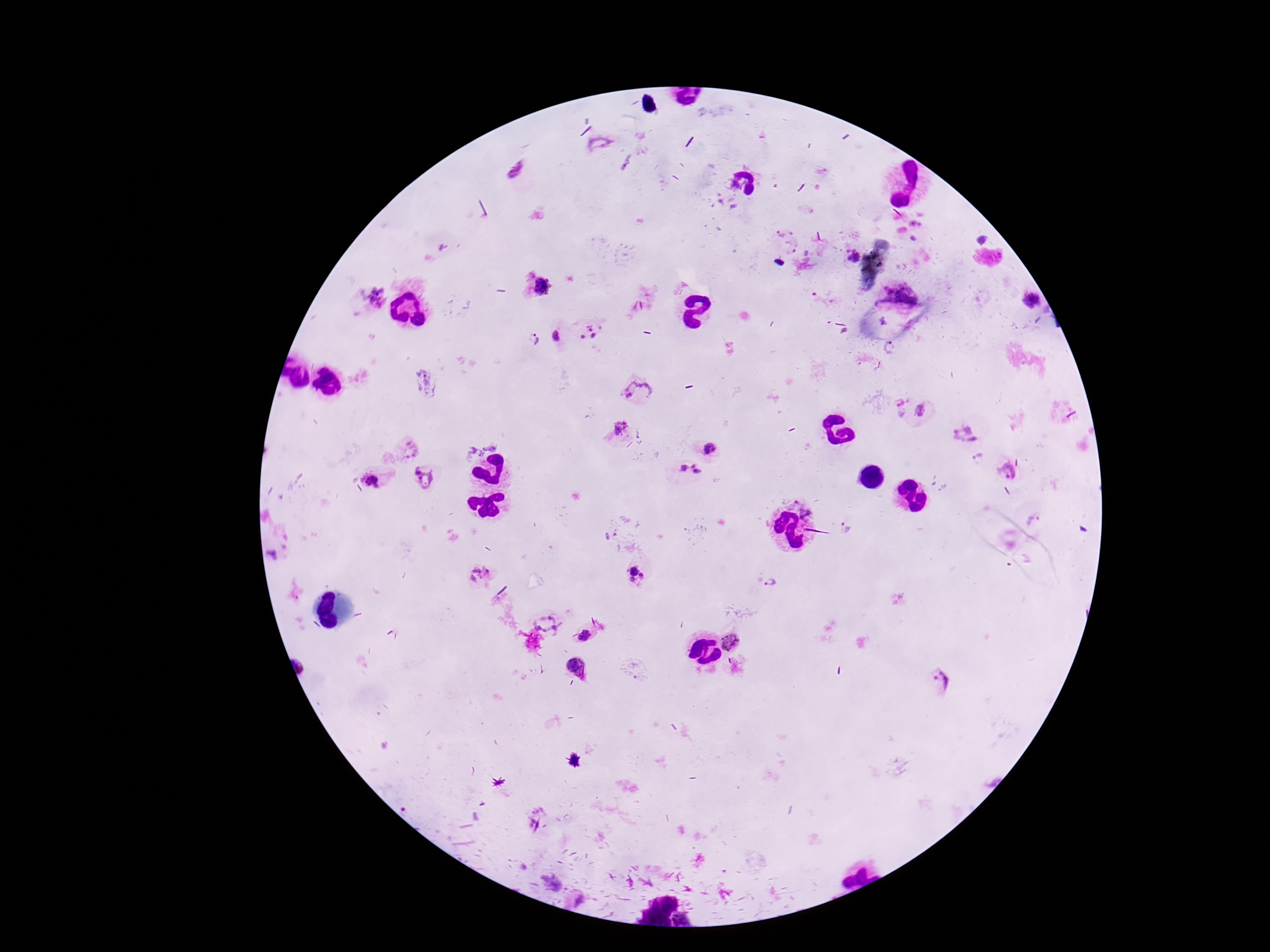
Approximate centers as {x, y} in pixels.
Summary:
  - Plasmodium parasite locations: {518, 171}, {984, 237}, {787, 243}, {851, 257}, {540, 287}, {375, 297}, {1031, 300}, {590, 331}, {557, 336}, {536, 339}, {889, 348}, {637, 390}, {901, 406}, {923, 411}, {621, 428}, {964, 433}, {407, 447}, {713, 449}, {979, 458}, {1006, 469}, {689, 473}, {424, 478}, {371, 481}, {847, 528}, {638, 574}, {480, 576}, {772, 584}, {549, 622}, {583, 635}, {731, 643}, {578, 668}, {943, 681}
  - Magnification: 100x
  - Preparation: thick blood smear
  - Stain: Giemsa
  - Image size: 1270×952 pixels
  - Patient malaria status: positive
  - Field of view: one from this slide
  - Capture: smartphone camera through the microscope eyepiece